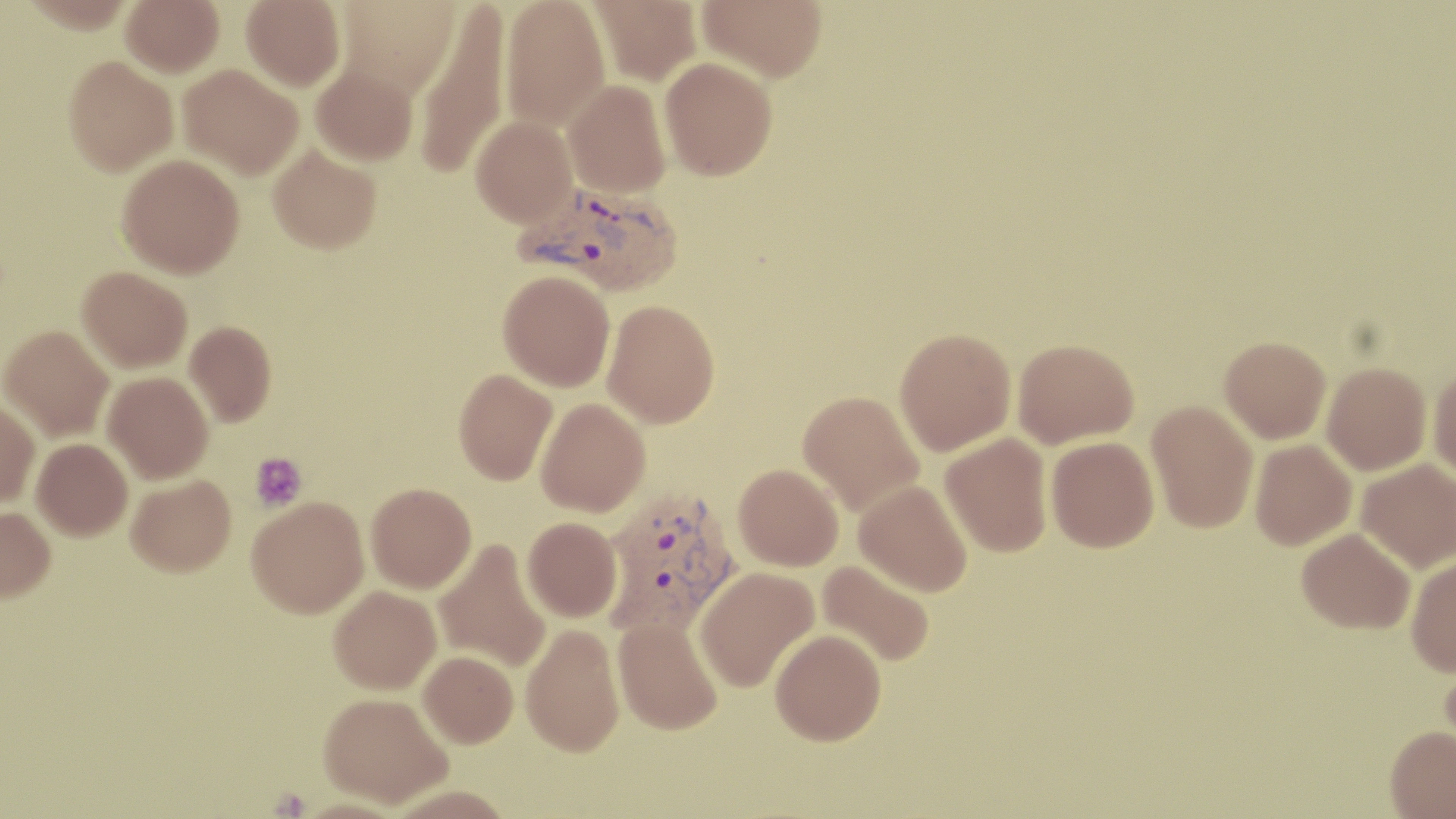

Plasmodium vivax-infected red blood cell locations = approximate bounding boxes as (x1,y1)-(x2,y2) corner pairs in pixels: (515,182)-(683,295), (599,487)-(740,637)
slide-level diagnosis = Plasmodium vivax
preparation = thin blood film
uninfected red blood cell locations = approximate bounding boxes as (x1,y1)-(x2,y2) corner pairs in pixels: (18,0)-(136,33), (121,0)-(224,77), (241,0)-(346,91), (335,0)-(463,98), (500,0)-(611,131), (590,0)-(702,85), (698,0)-(828,81), (414,4)-(511,181), (63,55)-(178,175), (660,57)-(777,180), (311,62)-(418,166), (178,64)-(303,179), (563,80)-(671,197), (471,115)-(577,226), (268,145)-(381,254), (117,154)-(244,278), (78,266)-(192,371), (498,270)-(615,391), (603,299)-(720,428), (185,321)-(276,426), (1,325)-(114,441), (894,327)-(1016,456), (1219,336)-(1331,443), (1013,338)-(1139,448), (1322,362)-(1432,475), (1428,366)-(1456,484), (453,369)-(557,484), (103,371)-(213,483), (796,389)-(924,515), (0,397)-(40,506), (536,398)-(651,516), (1146,400)-(1259,533), (940,432)-(1053,557), (1045,436)-(1159,552), (32,438)-(133,540), (1249,439)-(1356,550), (1356,458)-(1456,572), (733,463)-(844,571), (126,475)-(236,576), (854,479)-(973,596), (366,482)-(476,593), (246,496)-(369,618), (0,506)-(56,602), (522,516)-(622,622), (1297,527)-(1415,634), (433,538)-(552,673), (1406,556)-(1456,676), (817,559)-(935,666), (694,566)-(819,692), (329,585)-(442,694), (613,616)-(723,735), (521,623)-(625,756), (770,628)-(886,745), (419,651)-(518,748), (1439,656)-(1456,767), (319,691)-(452,807), (1385,725)-(1456,818)
stain = May-Grünwald-Giemsa
modality = optical microscopy
image size = 1456×819 pixels
field of view = one of a larger specimen
magnification = 1000x
platelet locations = approximate bounding boxes as (x1,y1)-(x2,y2) corner pairs in pixels: (250,452)-(307,510)